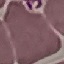
Summary:
  - Result: no malaria parasites detected
  - Stain: Giemsa
  - Image type: cell patch, automatically extracted from a larger field of view and resized to 64 × 64 pixels
  - Preparation: thin smear
  - Capture: smartphone camera at the microscope eyepiece